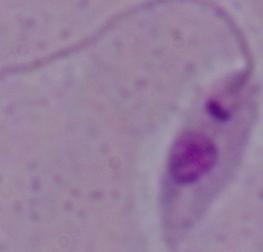
Summary:
  - Magnification: 1000x
  - Modality: micrograph
  - Identification: Leishmania